Report the malaria status of this cell.
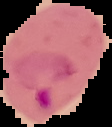

Parasitized.

Segmented cell region on a black background. Image is 112×127 pixels. From a thin blood smear.